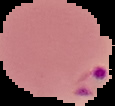

Summary:
  - Image size: 115×106 pixels
  - Preparation: thin blood smear
  - Image type: segmented cell region on a black background
  - Result: malaria parasites identified